Name the cell type shown.
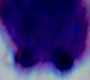

This is a leukocyte.

modality = micrograph
magnification = 1000x